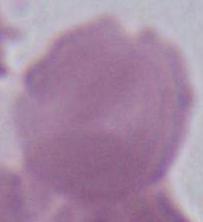
Summary:
  - Magnification: 1000x
  - Modality: micrograph
  - Identification: red blood cell